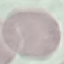
Summary:
  - Malaria status: uninfected
  - Stain: Giemsa
  - Image type: cell patch, automatically extracted from a larger field of view and resized to 64 × 64 pixels
  - Capture: smartphone through the microscope eyepiece
  - Preparation: thin smear